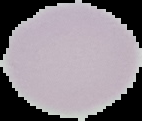

{
  "result": "no malaria parasites detected",
  "preparation": "thin blood film",
  "image_size": "142×121 pixels",
  "image_type": "segmented cell region on a black background"
}